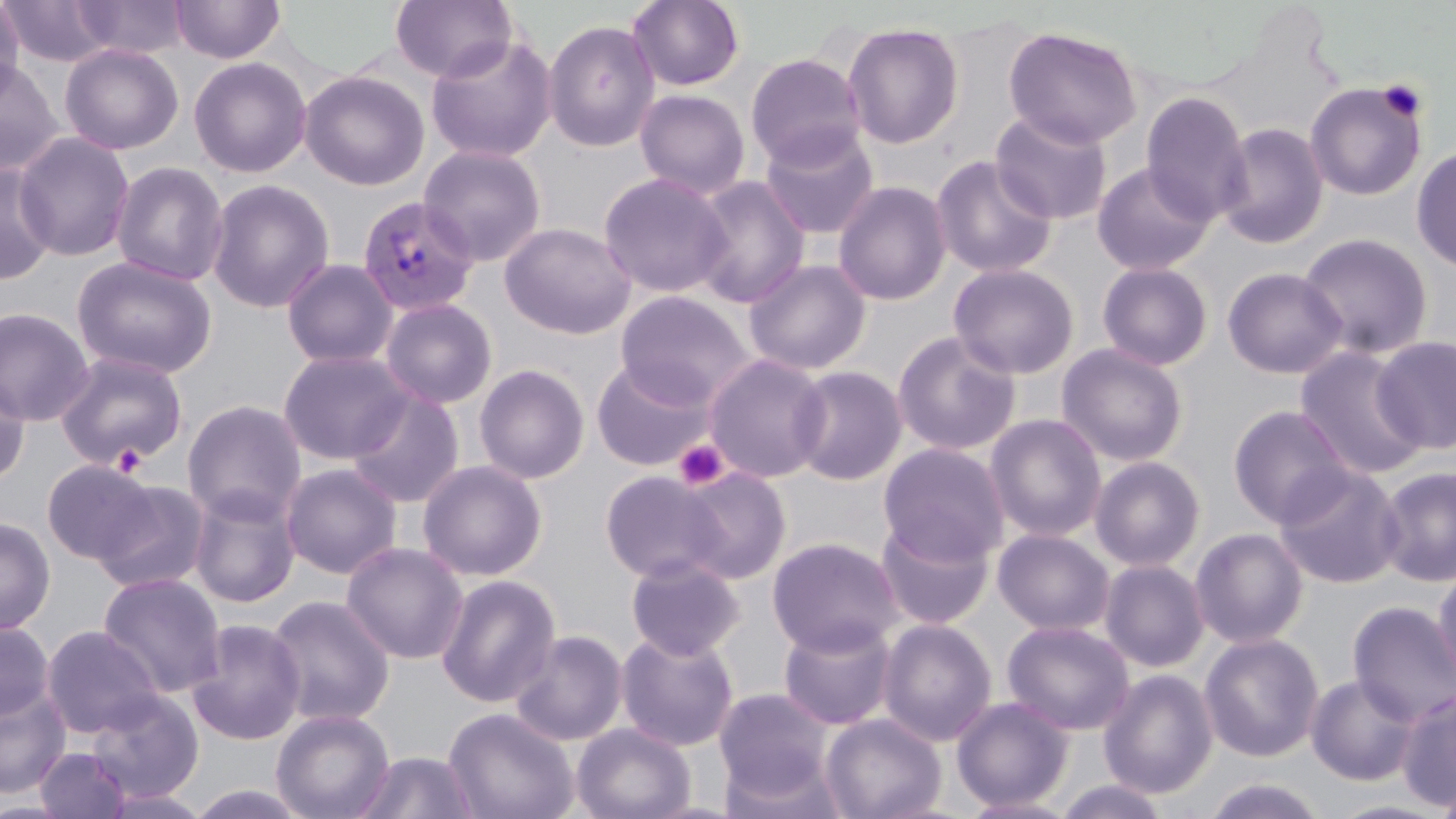

slide-level diagnosis = Plasmodium vivax
preparation = thin blood film
Plasmodium vivax-infected red blood cell locations = approximate bounding boxes as (x1,y1)-(x2,y2) corner pairs in pixels: (356,196)-(478,318)
field of view = single
uninfected red blood cell locations = approximate bounding boxes as (x1,y1)-(x2,y2) corner pairs in pixels: (71,0)-(189,59), (170,0)-(285,64), (390,0)-(517,83), (626,0)-(746,92), (0,1)-(24,104), (3,2)-(114,69), (542,19)-(660,153), (842,20)-(965,149), (1002,25)-(1143,149), (425,34)-(558,164), (60,43)-(183,155), (56,49)-(316,164), (745,52)-(866,168), (188,56)-(311,178), (0,58)-(63,175), (299,70)-(430,191), (1304,80)-(1428,201), (634,89)-(750,199), (1140,91)-(1253,226), (990,110)-(1114,225), (1214,122)-(1330,250), (759,124)-(880,240), (13,131)-(135,262), (418,144)-(547,267), (1411,146)-(1456,274), (930,154)-(1059,279), (0,161)-(58,286), (110,161)-(230,286), (1091,161)-(1216,275), (598,172)-(733,299), (689,176)-(810,309), (206,179)-(335,314), (832,180)-(952,307), (499,221)-(636,339), (1297,232)-(1434,360), (71,255)-(218,379), (281,258)-(399,369), (743,258)-(872,376), (1096,261)-(1214,371), (947,262)-(1080,379), (1222,267)-(1348,379), (614,291)-(756,408), (379,297)-(498,409), (0,307)-(95,426), (891,330)-(1022,456), (1372,335)-(1456,454), (1056,343)-(1189,467), (1294,346)-(1428,482), (278,348)-(413,464), (54,351)-(188,470), (703,353)-(831,483), (592,358)-(714,471), (473,363)-(590,484), (789,366)-(907,485), (0,369)-(31,487), (345,388)-(465,508), (182,399)-(307,524), (1227,404)-(1355,529), (985,414)-(1107,542), (877,442)-(1011,565), (1089,455)-(1206,571), (417,459)-(548,581), (41,460)-(156,565), (281,463)-(402,579), (1273,464)-(1404,588), (1376,465)-(1456,587), (675,466)-(792,584), (599,470)-(728,583), (90,479)-(211,593), (188,484)-(302,608), (0,516)-(56,635), (875,516)-(996,630), (1189,527)-(1309,648), (993,528)-(1115,636), (767,537)-(903,656), (341,541)-(469,664), (626,556)-(744,661), (1099,559)-(1209,672), (1431,563)-(1456,693), (97,572)-(226,699), (436,574)-(561,709), (265,595)-(396,727), (1347,601)-(1456,728), (778,617)-(898,730), (187,619)-(306,745), (878,619)-(997,746), (1002,620)-(1135,735), (0,621)-(55,722), (42,625)-(163,739), (509,630)-(628,746), (616,630)-(739,751), (1199,633)-(1324,762), (1098,669)-(1218,799), (1306,673)-(1422,786), (0,684)-(71,799), (714,688)-(834,801), (1396,689)-(1456,812), (86,690)-(204,803), (951,695)-(1073,811), (443,707)-(579,819), (271,708)-(395,819), (821,712)-(946,819), (571,722)-(696,819), (35,747)-(131,818), (355,750)-(479,818), (719,754)-(847,819), (1435,775)-(1456,819), (1201,777)-(1330,818), (1053,779)-(1171,819), (184,784)-(314,819), (95,786)-(214,818), (959,796)-(1080,818), (1324,798)-(1452,818)
image size = 1456×819 pixels
modality = light microscopy
magnification = 1000x
platelet locations = approximate bounding boxes as (x1,y1)-(x2,y2) corner pairs in pixels: (1376,79)-(1428,122), (673,439)-(729,490), (111,443)-(148,475)
stain = May-Grünwald-Giemsa